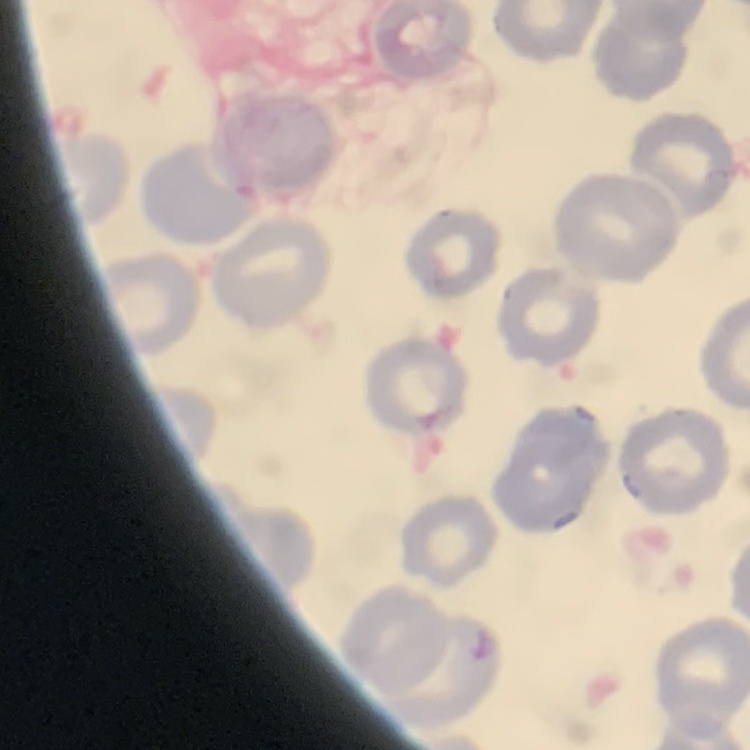
The erythrocytes show no rouleaux formation. Stained with either Field's or Giemsa. One tile cut from a larger photomicrograph. Thin blood smear.